Report the malaria status of this cell.
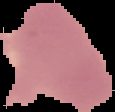

It is uninfected.

preparation = thin blood film
image type = segmented cell region on a black background
image size = 115×112 pixels